Give the position of every malaria parasite.
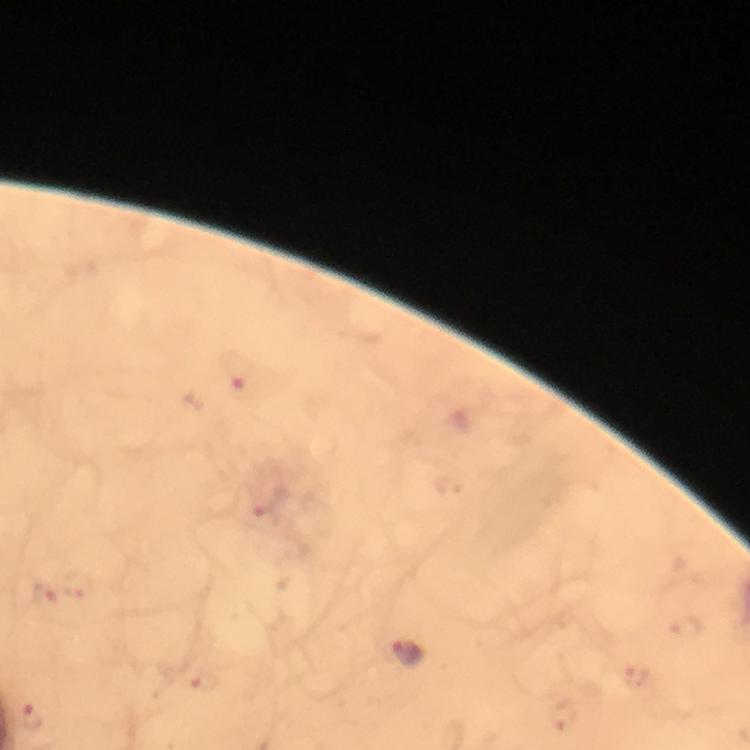
Approximate centers as [x, y] in pixels.
Malaria parasites: [239, 372], [267, 507], [42, 596], [684, 630], [410, 652], [638, 679], [202, 680], [31, 716], [564, 720].

{
  "stain": "Giemsa",
  "capture": "smartphone camera through the microscope",
  "context": "from a malaria diagnostic workup",
  "image_size": "750×750 pixels",
  "magnification": "100x",
  "preparation": "thick smear",
  "cropped_from": "one field of view",
  "immersion_oil": "used"
}